Point out each leukocyte.
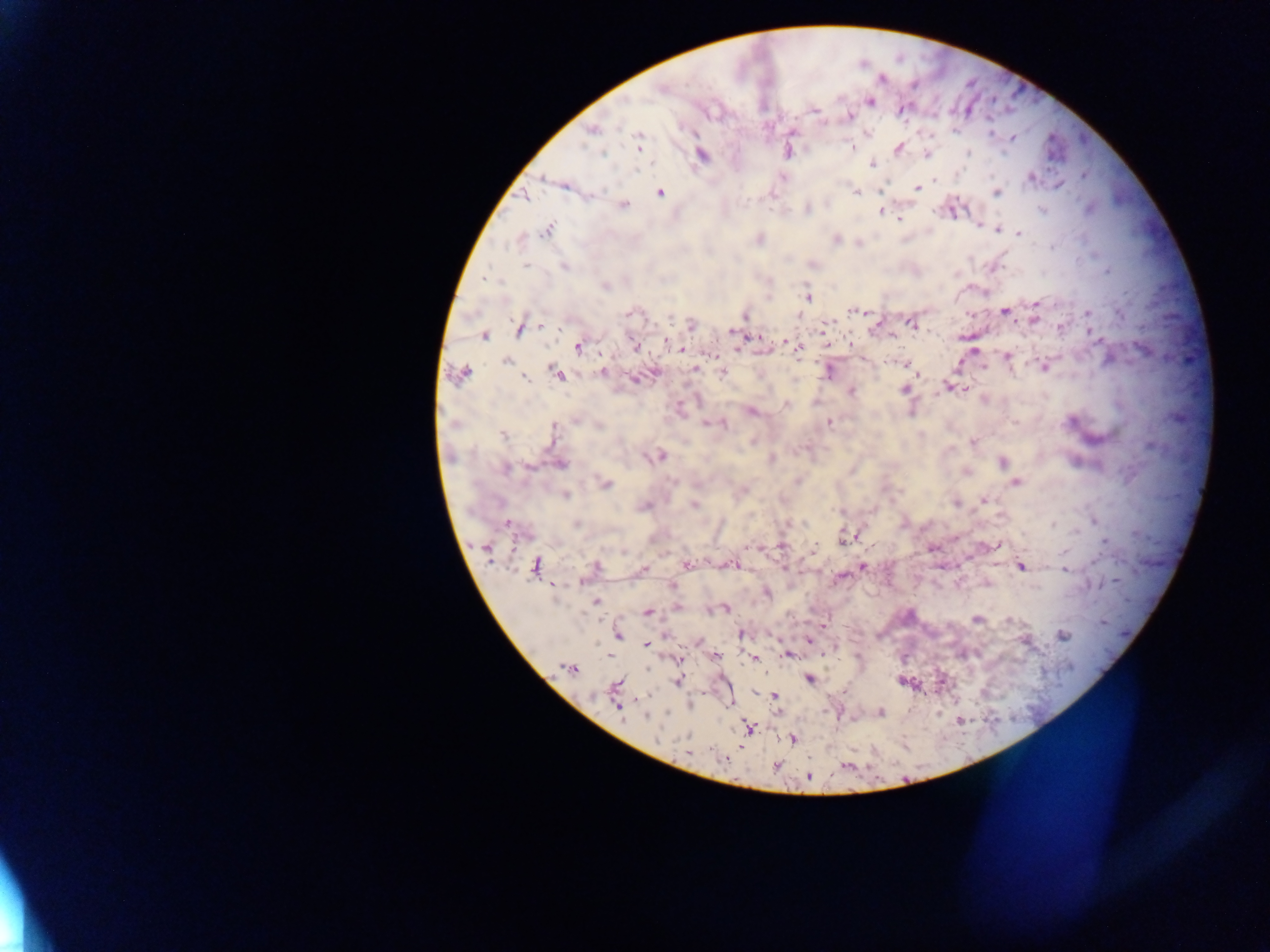
No leukocytes observed.

Approximate centers as (x, y) in pixels. Malaria parasite locations: (883, 79), (661, 89), (870, 102), (814, 111), (848, 117), (592, 130), (1013, 137), (638, 142), (852, 148), (899, 148), (969, 152), (602, 153), (702, 155), (872, 164), (543, 178), (1031, 178), (934, 180), (917, 188), (880, 190), (996, 192), (660, 193), (857, 193), (524, 196), (623, 206), (807, 209), (1042, 209), (881, 211), (899, 219), (980, 226), (548, 229), (999, 229), (1018, 233), (759, 239), (836, 239), (526, 266), (564, 267), (1107, 271), (485, 278), (605, 286), (808, 298), (1036, 303), (855, 311), (1004, 311), (1087, 313), (629, 314), (970, 315), (745, 316), (670, 317), (1034, 320), (877, 323), (912, 324), (541, 326), (691, 326), (824, 326), (1060, 327), (519, 329), (732, 331), (484, 336), (892, 336), (756, 337), (1097, 340), (667, 342), (788, 343), (635, 346), (578, 347), (678, 348), (738, 349), (797, 350), (973, 350), (711, 355), (1007, 357), (506, 362), (906, 365), (1044, 367), (695, 368), (983, 368), (829, 371), (602, 372), (461, 373), (723, 373), (557, 374), (919, 374), (525, 379), (634, 380), (946, 386), (954, 388), (905, 389), (964, 389), (851, 392), (786, 404), (751, 412), (575, 420), (829, 423), (707, 424), (724, 425), (599, 426), (554, 430), (503, 436), (972, 442), (660, 456), (772, 459), (1003, 462), (560, 464), (529, 467), (505, 470), (798, 481), (1016, 482), (606, 483), (566, 496), (984, 500), (956, 503), (694, 505), (643, 506), (507, 524), (576, 524), (1053, 524), (847, 538), (1105, 541), (998, 545), (780, 546), (747, 547), (486, 550), (813, 550), (687, 565), (730, 565), (535, 566), (1021, 566), (595, 567), (862, 567), (644, 568), (1116, 581), (672, 586), (766, 592), (596, 601), (678, 607), (726, 609), (648, 612), (977, 619), (1009, 620), (824, 624), (618, 634), (741, 634), (1062, 636), (808, 641), (647, 644), (787, 655), (718, 657), (755, 659), (679, 660), (569, 668), (808, 679), (677, 681), (616, 685), (774, 696), (619, 707), (880, 712), (647, 717), (749, 728), (792, 740), (688, 752), (723, 760), (809, 777). Mobile-phone photograph taken through the microscope. Thick blood smear. Single field of view. Sample from Ghana. Image is 1270×952 pixels.